Name the parasite shown.
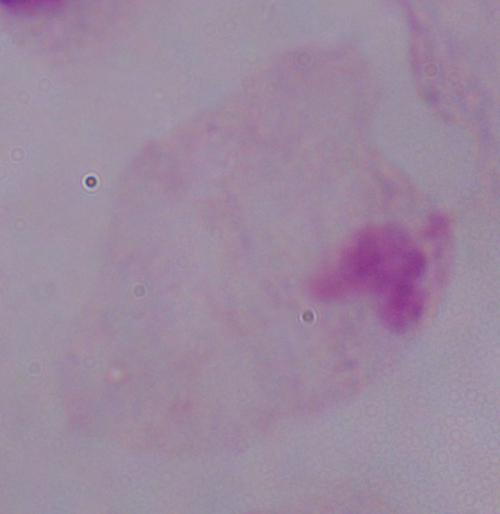
A trichomonad.

1000x magnification. Micrograph.